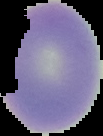
preparation: thin blood smear
image_type: cell region segmented out of the field of view; surrounding area masked to black
image_size: 103×136 pixels
malaria_status: uninfected